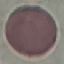 Malaria status: uninfected. Thin smear of blood. Automatically extracted cell patch, resized to 64 × 64 pixels. Giemsa stain. Photographed with a smartphone camera at the microscope eyepiece.